Assess this cell for malaria.
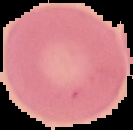
Uninfected.

image size = 133×130 pixels
image type = segmented cell region with the area outside set to black
preparation = thin blood film